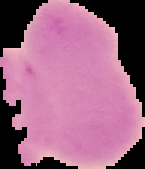

image size = 145×169 pixels
preparation = thin blood film
malaria status = uninfected
image type = segmented cell region on a black background